Evaluate for Plasmodium parasites.
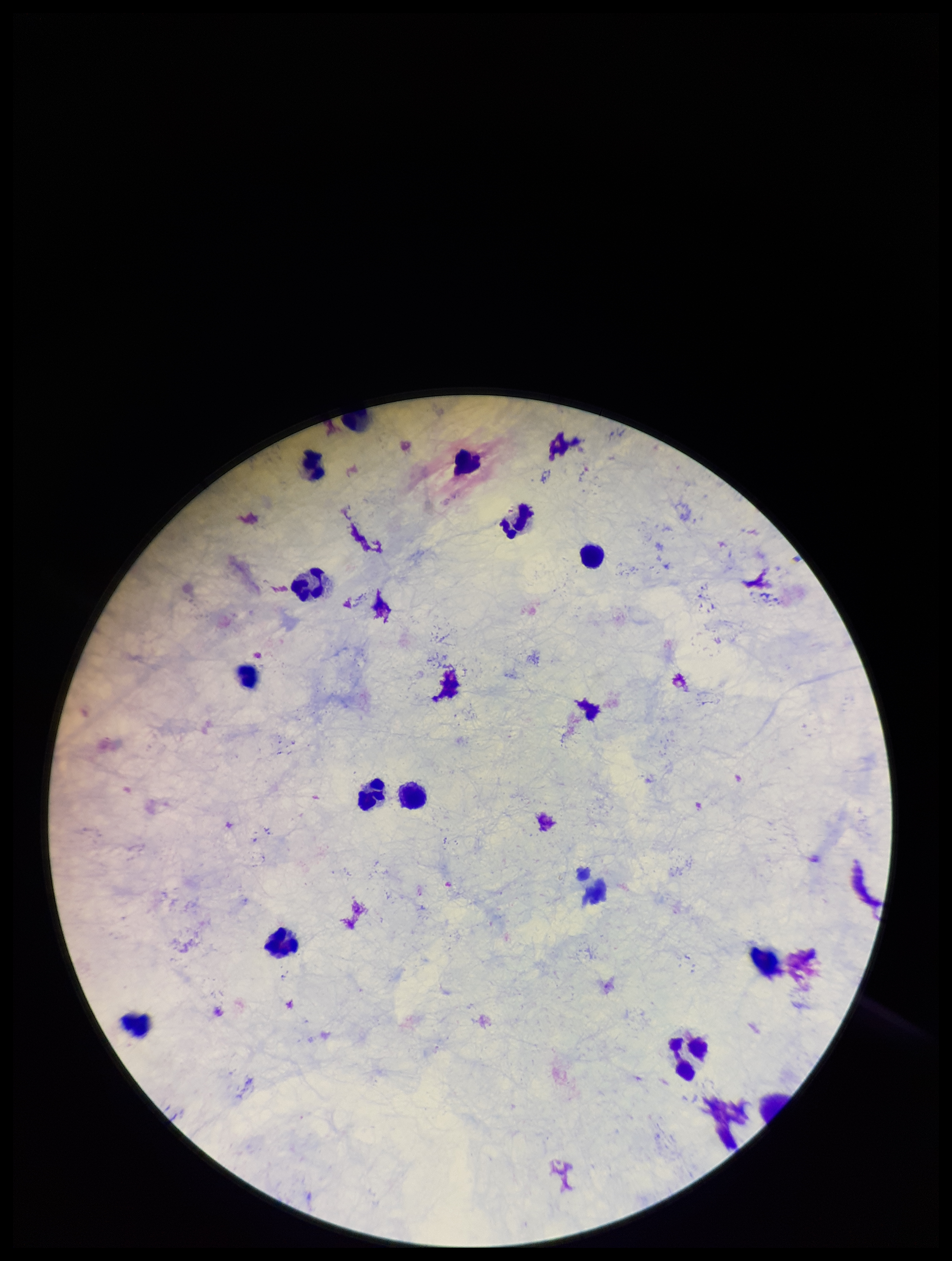
None identified.

Summary:
  - Parasite count: 0
  - Patient malaria status: negative
  - Leukocyte count: 13
  - Field of view: one from this slide
  - Capture: smartphone photograph through the microscope eyepiece
  - Image size: 952×1261 pixels
  - Stain: Giemsa
  - Preparation: thick